Locate every blood parasite and identify its species.
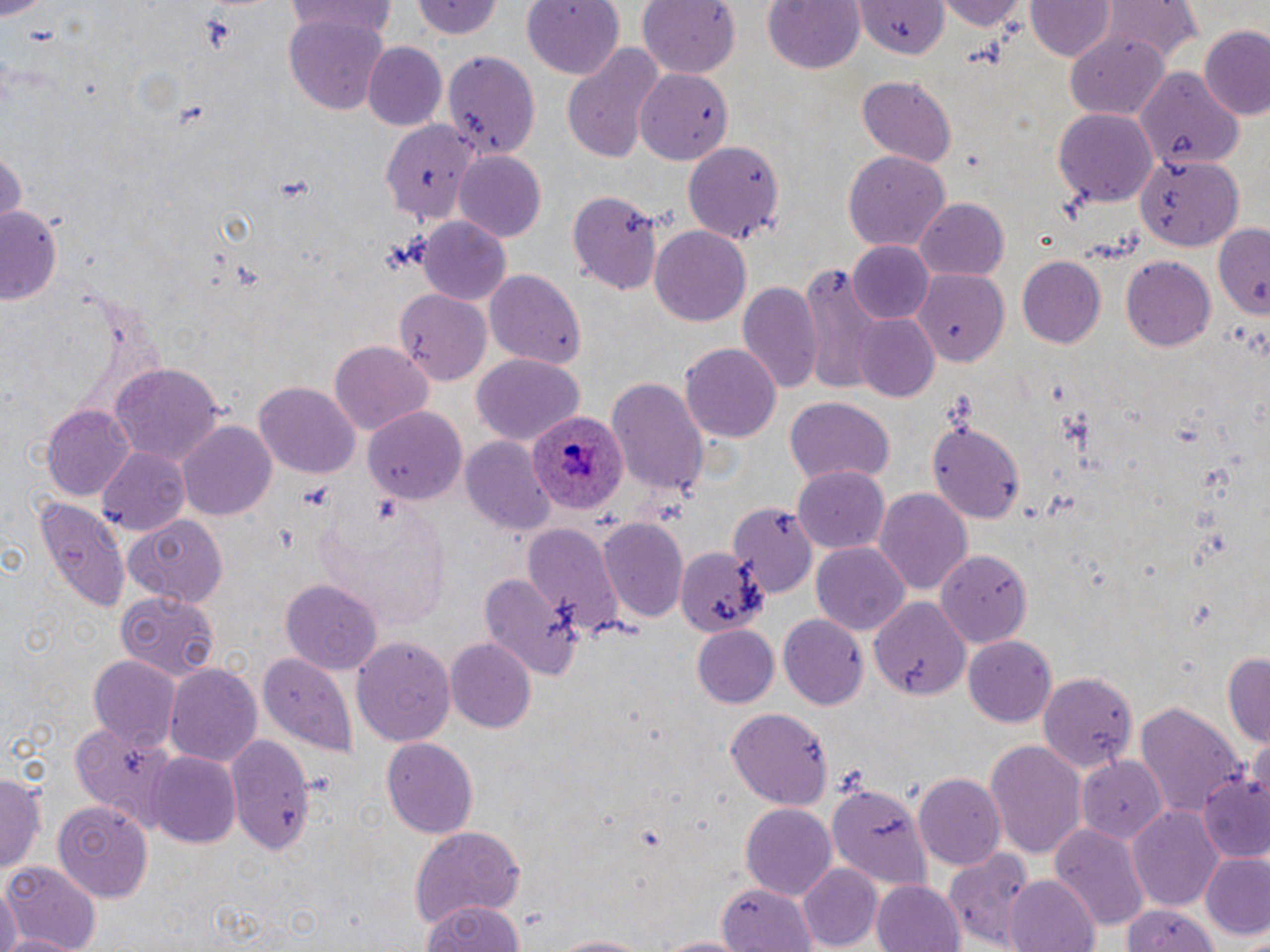

Approximate bounding boxes as (x1, y1, x2, y2) in pixels.
Plasmodium ovale-infected red blood cells: (528, 414, 626, 514).
No Plasmodium falciparum, Plasmodium malariae, Plasmodium vivax, Babesia divergens, or Trypanosoma brucei observed.

Uninfected red blood cell locations: (522, 0, 625, 81), (639, 0, 741, 75), (763, 0, 866, 75), (936, 0, 1024, 30), (1099, 0, 1202, 63), (284, 1, 400, 39), (415, 1, 507, 42), (859, 1, 942, 57), (1027, 2, 1114, 62), (284, 14, 391, 114), (1199, 27, 1270, 122), (1062, 32, 1172, 123), (361, 43, 447, 131), (561, 43, 664, 164), (442, 50, 541, 159), (637, 67, 736, 164), (1134, 70, 1246, 169), (857, 76, 958, 166), (1052, 108, 1159, 207), (378, 118, 478, 231), (681, 141, 785, 242), (0, 145, 25, 229), (843, 150, 949, 256), (454, 153, 547, 243), (1134, 153, 1242, 251), (568, 188, 664, 297), (915, 197, 1009, 278), (3, 205, 64, 306), (417, 217, 513, 307), (1208, 220, 1270, 318), (648, 225, 751, 327), (848, 242, 935, 323), (1120, 255, 1215, 350), (1017, 256, 1104, 347), (797, 264, 887, 394), (484, 267, 586, 367), (913, 268, 1008, 364), (738, 280, 823, 394), (394, 289, 491, 385), (854, 314, 940, 402), (328, 341, 433, 436), (680, 342, 781, 444), (472, 354, 582, 445), (108, 361, 224, 464), (608, 376, 708, 501), (254, 383, 360, 476), (787, 399, 894, 485), (40, 404, 136, 501), (363, 407, 467, 505), (179, 420, 277, 523), (928, 422, 1024, 520), (462, 438, 553, 535), (97, 449, 189, 534), (793, 467, 889, 552), (874, 487, 973, 594), (29, 496, 131, 614), (728, 500, 814, 595), (125, 516, 225, 607), (598, 517, 689, 623), (520, 523, 625, 639), (675, 543, 765, 638), (811, 543, 909, 636), (934, 546, 1034, 651), (482, 572, 584, 678), (281, 579, 382, 673), (115, 589, 219, 680), (866, 596, 972, 696), (777, 612, 868, 710), (692, 625, 779, 709), (352, 635, 455, 744), (963, 637, 1057, 728), (445, 638, 536, 732), (1222, 650, 1270, 748), (256, 652, 359, 758), (87, 655, 181, 747), (164, 660, 261, 765), (1036, 670, 1137, 775), (1135, 701, 1247, 818), (725, 708, 834, 809), (69, 721, 176, 827), (226, 735, 315, 857), (381, 736, 479, 836), (985, 739, 1086, 858), (149, 753, 242, 849), (1074, 757, 1165, 845), (0, 768, 44, 881), (1199, 771, 1270, 862), (914, 773, 1006, 871), (828, 782, 930, 890), (52, 798, 153, 900), (1127, 803, 1225, 910), (739, 804, 836, 901), (1050, 825, 1149, 929), (408, 827, 525, 928), (943, 846, 1036, 949), (1201, 852, 1270, 941), (3, 862, 102, 951), (796, 864, 881, 948), (1006, 875, 1100, 952), (871, 879, 965, 952), (0, 882, 20, 952), (718, 882, 815, 951), (419, 898, 526, 952), (1120, 900, 1221, 952), (542, 932, 659, 951), (647, 933, 747, 951). Slide-level diagnosis: Plasmodium ovale. Optical microscopy. Thin blood smear. May-Grünwald-Giemsa-stained preparation. Image is 1270×952 pixels. 1000x magnification. Single field of view.